Report the malaria status of this cell.
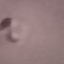
It is parasitized.

{
  "stain": "Giemsa",
  "image_type": "automatically extracted cell patch, resized to 64 × 64 pixels",
  "capture": "smartphone camera at the microscope eyepiece",
  "preparation": "thin smear"
}